Evaluate for parasitized red blood cells.
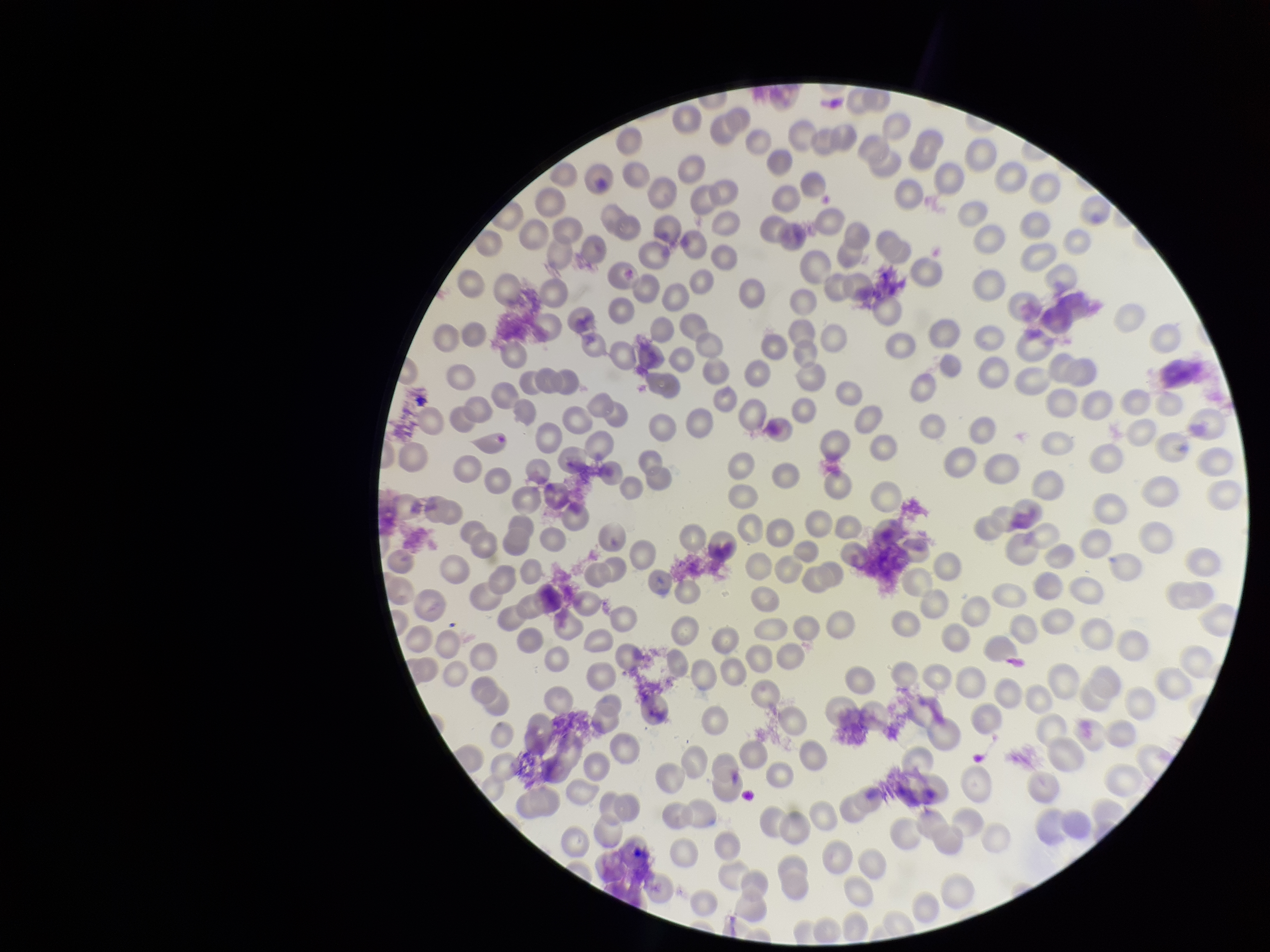

None seen.

Patient malaria status: negative. Red blood cell count: 228. Image is 1270×952 pixels. One field from this slide. Smartphone photograph taken through the eyepiece of a microscope. Preparation: thin smear. Stained with Giemsa. Parasitized red blood cell count: 0.